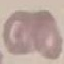 Malaria status: uninfected. Automatically extracted cell patch, resized to 64 × 64 pixels. Photographed with a smartphone camera at the microscope eyepiece. Thin blood film. Giemsa stain.